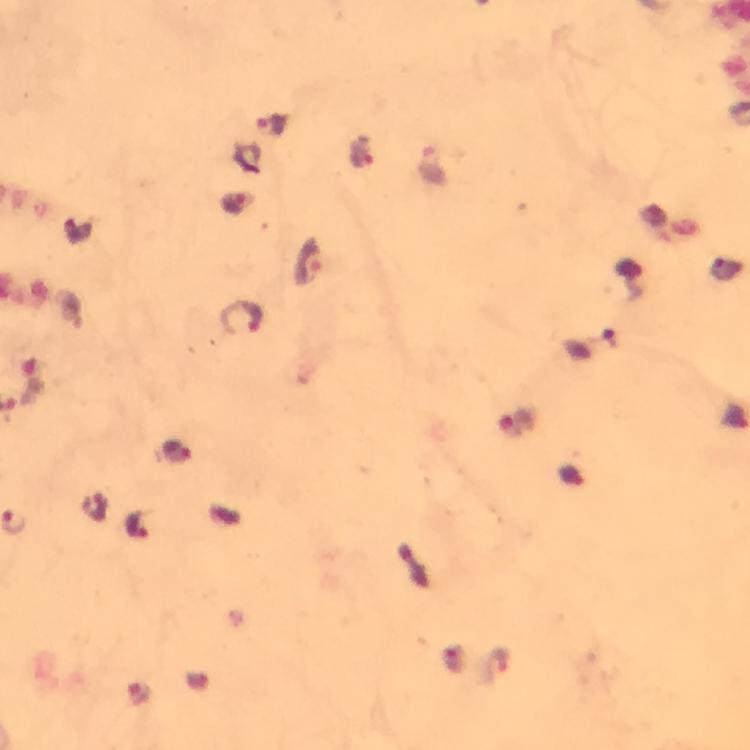

Approximate centers as [x, y] in pixels.
Summary:
  - Plasmodium parasite locations: [274, 124], [362, 150], [234, 202], [307, 261], [243, 316], [31, 380], [518, 421], [177, 451], [138, 526], [498, 665]
  - Stain: Giemsa
  - Context: from a malaria diagnostic workup
  - Capture: smartphone photograph through a microscope
  - Cropped from: one field of view
  - Image size: 750×750 pixels
  - Immersion oil: applied
  - Preparation: thick blood smear
  - Magnification: 100x